Name the parasite shown.
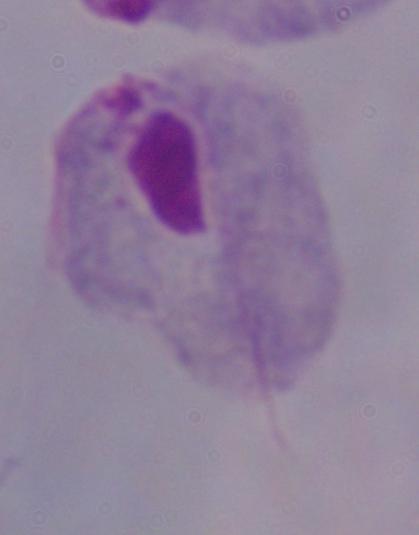

This is a trichomonad.

Summary:
  - Modality: micrograph
  - Magnification: 1000x